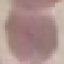 Result: negative for malaria parasites. Cell patch, automatically extracted from a larger field of view and resized to 64 × 64 pixels. Giemsa stain. Thin smear of blood. Acquired by smartphone through the microscope eyepiece.